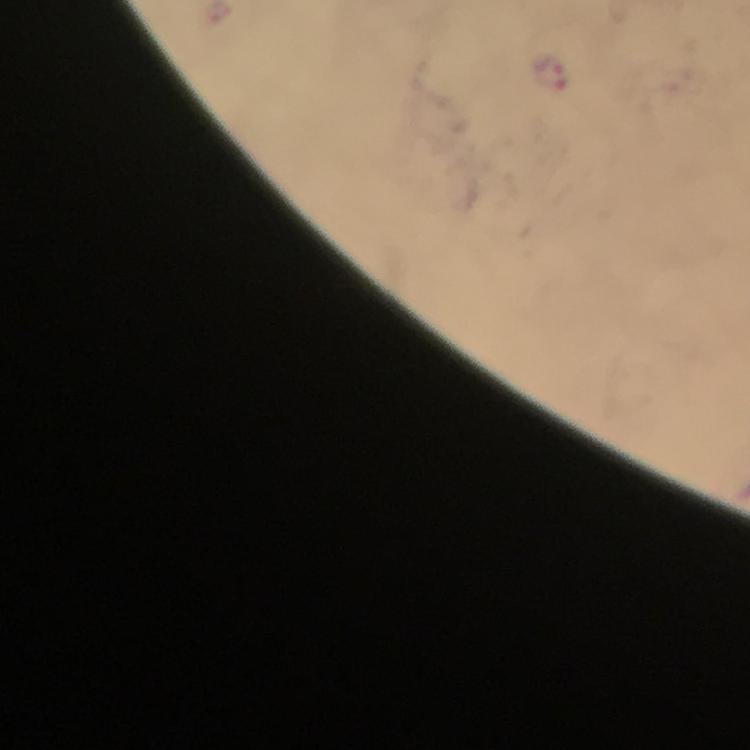
Approximate object centers, in pixels from the top-left corner.
Summary:
  - Plasmodium parasite locations: (x=550, y=74)
  - Capture: smartphone camera through the microscope
  - Immersion oil: used
  - Stain: Giemsa
  - Image size: 750×750 pixels
  - Preparation: thick smear
  - Cropped from: a single field of view
  - Magnification: 100x
  - Context: from a diagnostic examination for malaria